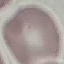
Summary:
  - Result: negative for malaria parasites
  - Capture: smartphone through the microscope eyepiece
  - Stain: Giemsa
  - Preparation: thin smear
  - Image type: cell patch, automatically extracted from a larger field of view and resized to 64 × 64 pixels